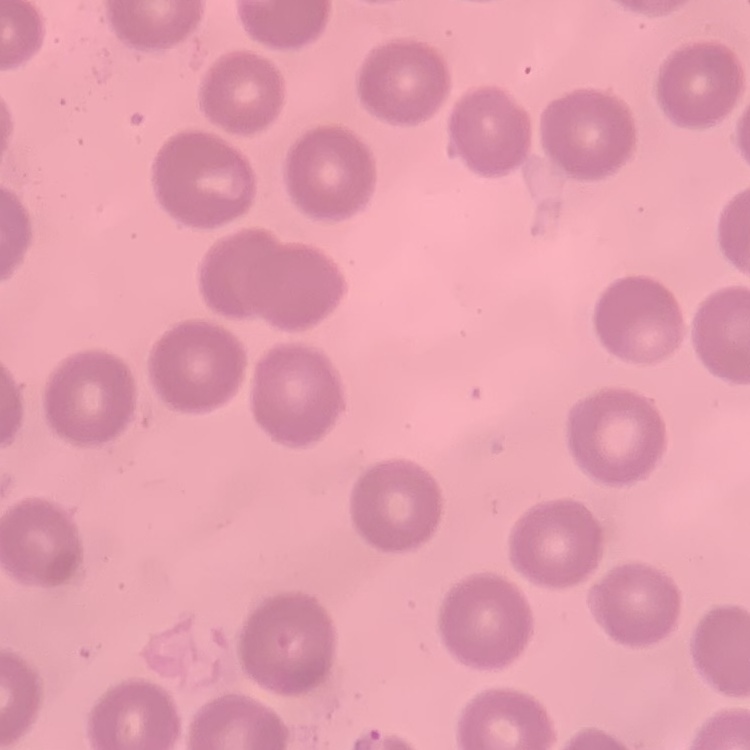

erythrocyte morphology = no rouleaux formation
image type = one tile cut from a larger photomicrograph
stain = Field's or Giemsa
preparation = thin blood film